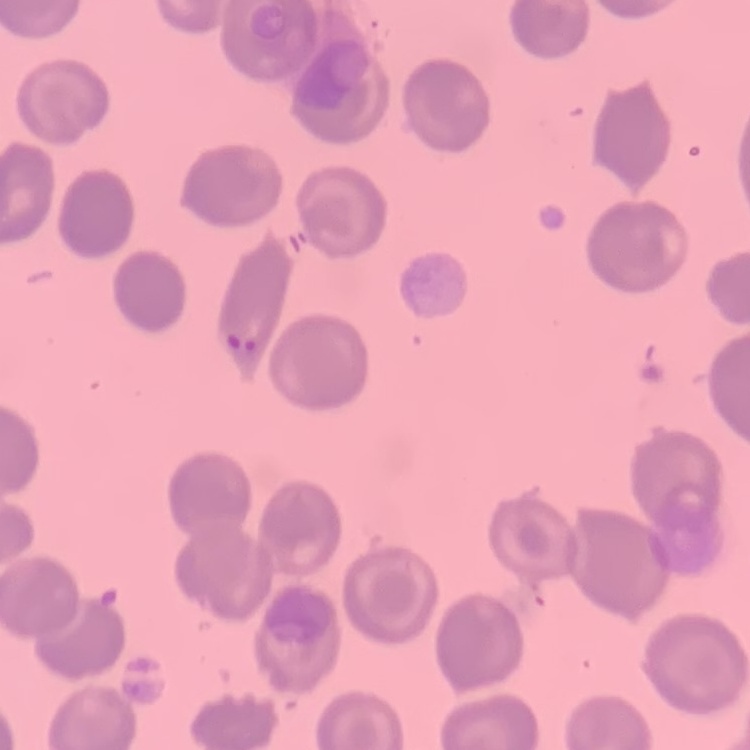 The erythrocytes exhibit no rouleaux formation. Field's or Giemsa stain. Square crop of a larger photomicrograph. Thin peripheral smear.